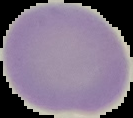

preparation = thin blood film
image size = 133×118 pixels
image type = segmented cell region with the area outside set to black
malaria status = uninfected